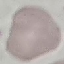 Malaria status: uninfected. Thin blood smear. Acquired by smartphone through the microscope eyepiece. Cell patch, automatically extracted from a larger field of view and resized to 64 × 64 pixels. Giemsa stain.